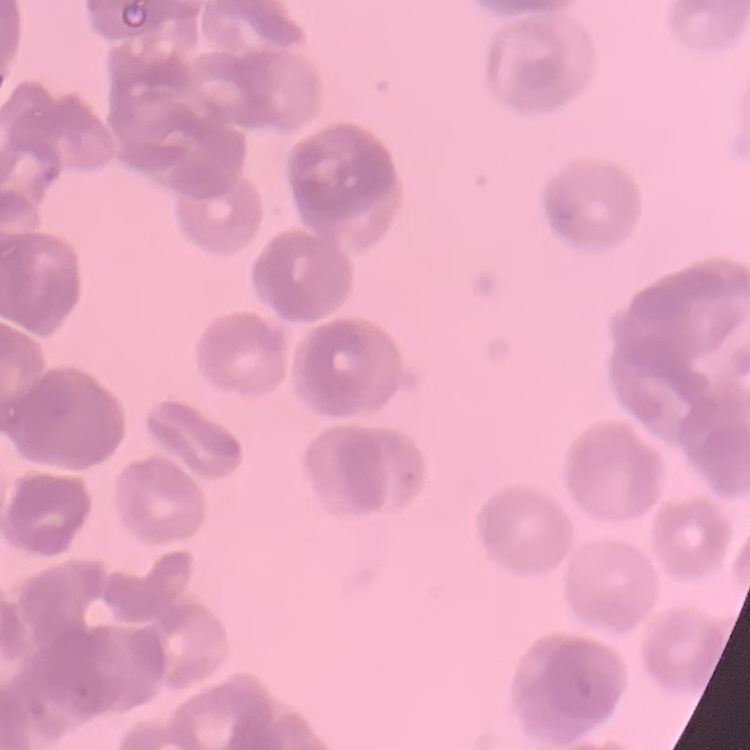
The erythrocytes show rouleaux formation. Thin blood smear. Field's or Giemsa stain. One tile cut from a larger photomicrograph.